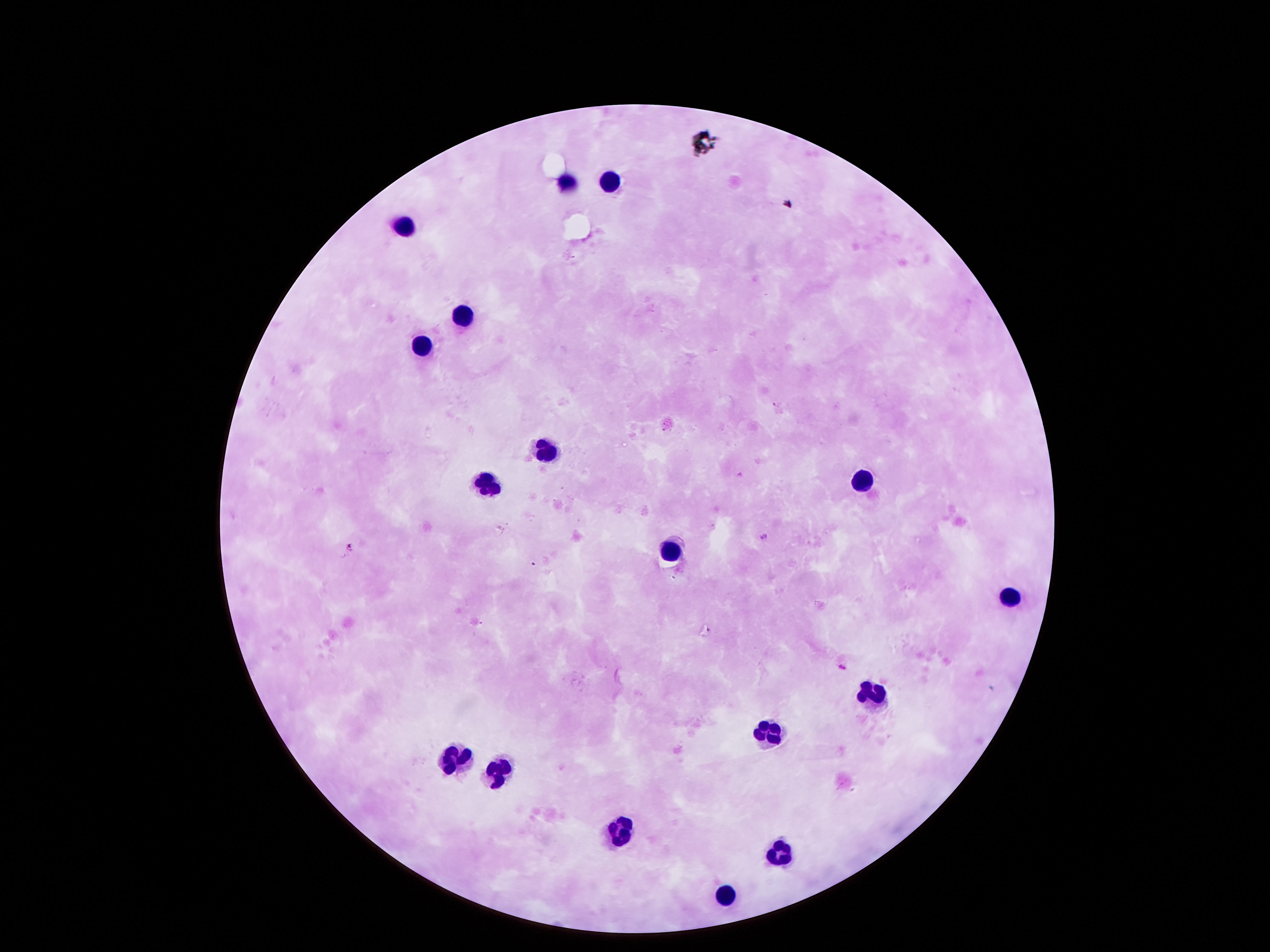
field of view = single
patient malaria status = not infected
capture = smartphone camera through the microscope eyepiece
stain = Giemsa
image size = 1270×952 pixels
preparation = thick blood film
magnification = 100x
leukocyte locations = approximate centers as [x, y] in pixels: [607, 180], [567, 182], [403, 226], [459, 310], [423, 345], [547, 449], [863, 480], [483, 482], [667, 549], [1007, 598], [875, 691], [769, 731], [453, 760], [497, 771], [615, 831], [783, 847], [725, 893]